Identify the cell.
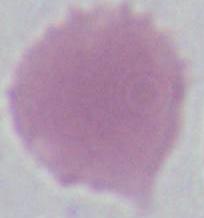

An erythrocyte.

magnification = 1000x
modality = micrograph